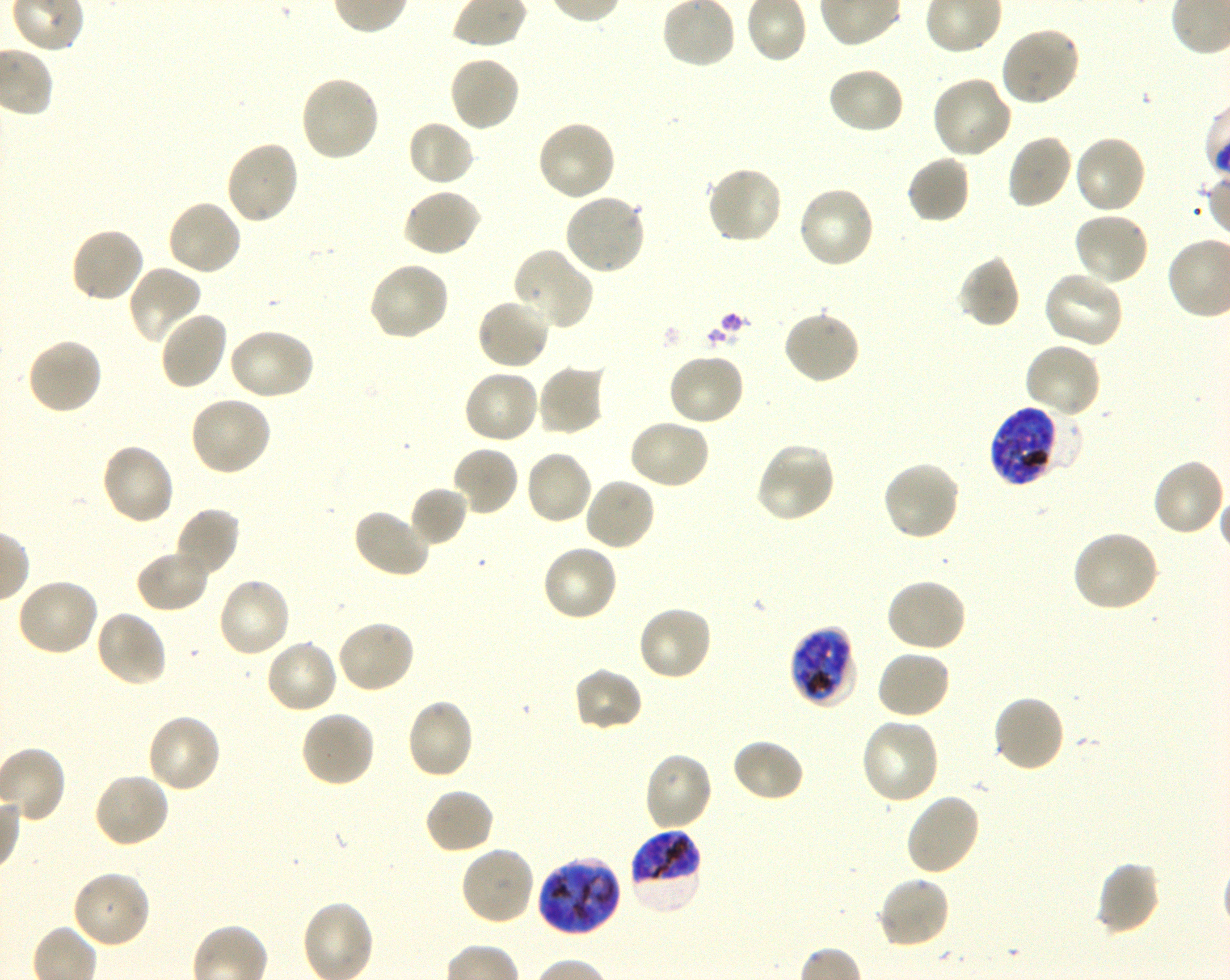
Not every red blood cell is marked. A life-cycle stage — or a range of stages, where the recorded stages span more than one — follows each staged infected red blood cell.
locations of uninfected red blood cells = approximate bounding boxes as {x1, y1, x2, y2} in pixels: {999, 25, 1082, 107}, {447, 54, 522, 133}, {826, 66, 906, 135}, {299, 75, 380, 164}, {931, 75, 1014, 160}, {406, 118, 476, 187}, {536, 120, 617, 203}, {1005, 133, 1074, 211}, {1073, 134, 1149, 215}, {223, 139, 300, 226}, {906, 154, 971, 225}, {705, 165, 785, 245}, {796, 185, 877, 270}, {402, 187, 483, 258}, {562, 192, 646, 275}, {166, 199, 243, 277}, {1073, 211, 1151, 287}, {69, 225, 145, 304}, {514, 248, 594, 331}, {956, 255, 1021, 329}, {367, 260, 451, 342}, {127, 265, 202, 346}, {1041, 270, 1124, 350}, {476, 297, 552, 372}, {782, 309, 862, 386}, {158, 310, 228, 391}, {226, 327, 316, 402}, {25, 337, 103, 416}, {1023, 341, 1103, 418}, {666, 351, 746, 427}, {536, 363, 607, 436}, {463, 368, 541, 446}, {188, 394, 273, 477}, {627, 418, 711, 490}, {98, 443, 177, 526}, {755, 443, 838, 523}, {451, 445, 520, 517}, {523, 448, 594, 526}, {1151, 458, 1227, 538}, {881, 460, 962, 542}, {583, 476, 657, 552}, {409, 486, 468, 547}, {172, 507, 241, 580}, {351, 507, 434, 579}, {1070, 530, 1160, 614}, {541, 544, 619, 623}, {134, 548, 211, 614}, {216, 576, 292, 659}, {14, 577, 100, 658}, {885, 577, 968, 652}, {636, 604, 714, 682}, {94, 611, 169, 689}, {336, 619, 417, 695}, {265, 639, 338, 715}, {876, 649, 952, 721}, {572, 666, 644, 733}, {992, 694, 1066, 773}, {404, 698, 476, 781}, {299, 710, 376, 788}, {146, 712, 222, 794}, {859, 716, 940, 806}, {730, 738, 806, 803}, {642, 750, 715, 832}, {93, 771, 172, 849}, {423, 787, 495, 855}, {904, 793, 981, 877}, {459, 845, 535, 927}, {1094, 860, 1161, 937}, {71, 868, 152, 949}, {876, 875, 952, 950}
donor blood group = O+
stain = Giemsa
culture = in-vitro Plasmodium falciparum strain 3D7, shaking
locations of infected red blood cells = approximate bounding boxes as {x1, y1, x2, y2} in pixels: {990, 406, 1067, 486} late trophozoite to late schizont; {789, 626, 856, 706} late trophozoite to late schizont; {627, 828, 703, 915} late trophozoite to late schizont; {536, 857, 622, 937} late trophozoite to early schizont
objective = 100x, oil immersion, numerical aperture 1.30
field of view = one from this slide
preparation = thin blood smear
image size = 1230×980 pixels